Describe the morphology of the red blood cells.
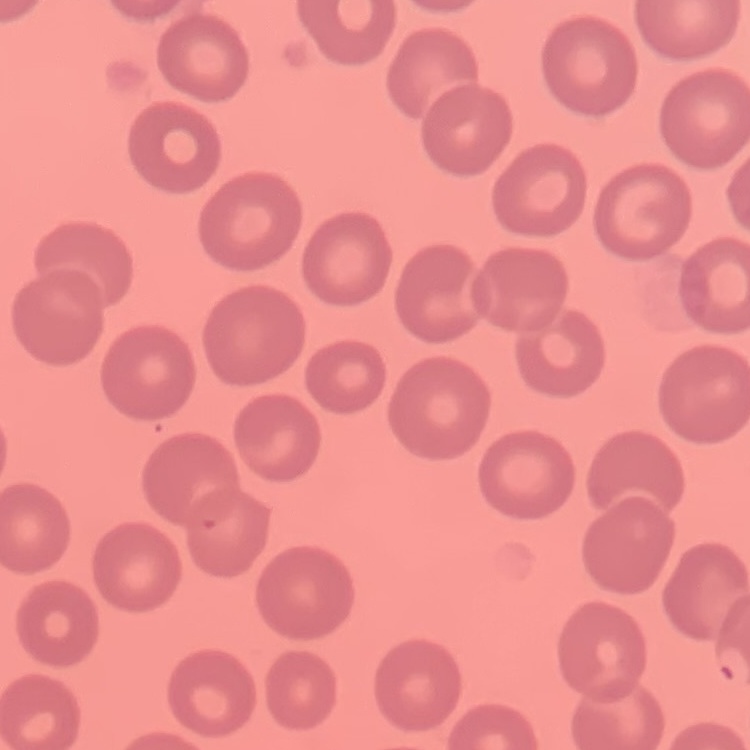

No rouleaux formation.

{
  "image_type": "one tile cut from a larger photomicrograph",
  "preparation": "thin blood film",
  "stain": "Field's or Giemsa"
}